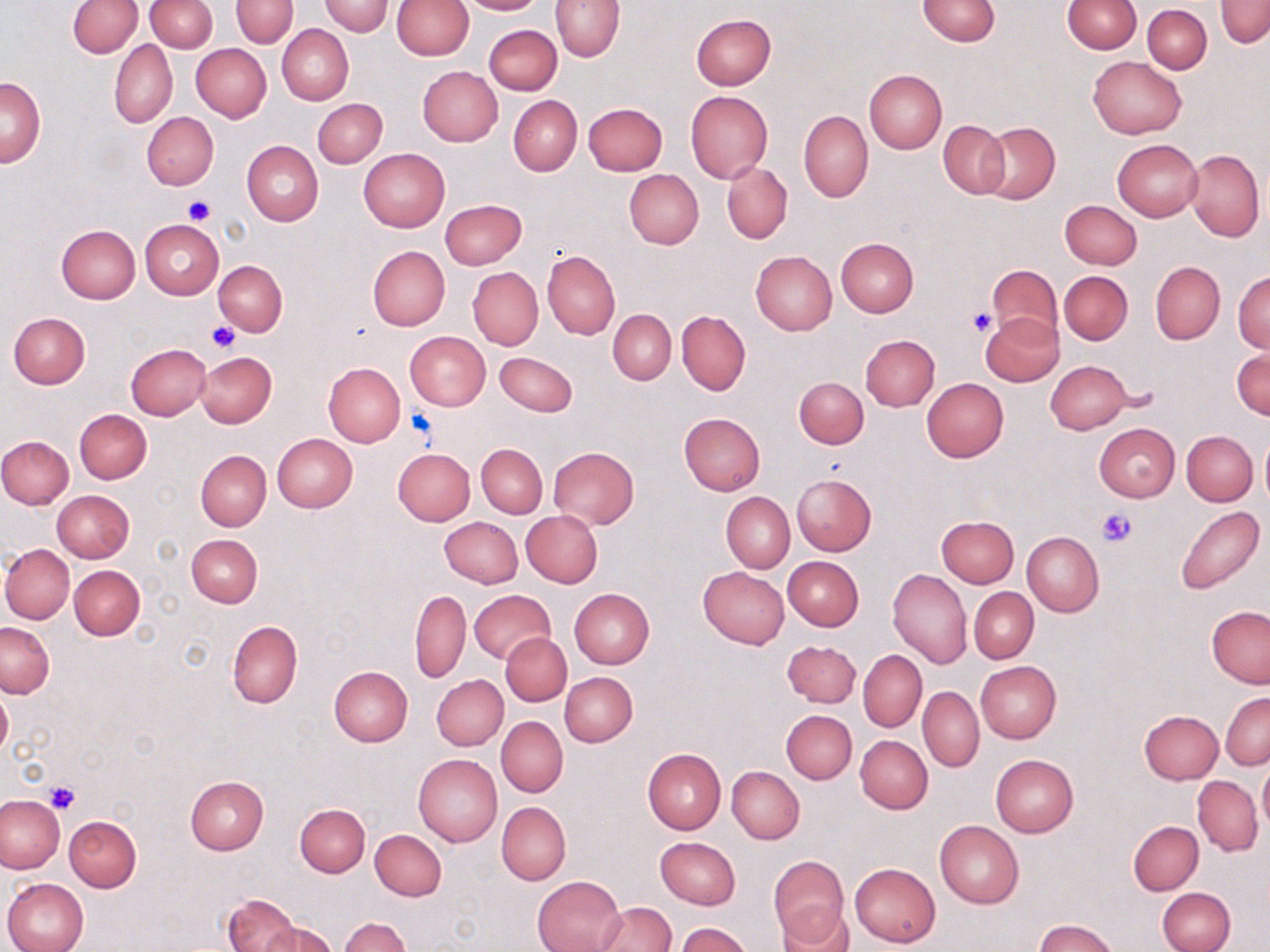

Approximate bounding boxes as named x1/y1/x2/y2 corners in pixels. Platelet locations: (x1=183, y1=197, x2=215, y2=224), (x1=968, y1=307, x2=997, y2=335), (x1=207, y1=321, x2=241, y2=352), (x1=406, y1=410, x2=435, y2=440), (x1=1097, y1=509, x2=1135, y2=548), (x1=42, y1=779, x2=82, y2=815). Uninfected red blood cell locations: (x1=145, y1=0, x2=217, y2=53), (x1=231, y1=0, x2=298, y2=48), (x1=460, y1=0, x2=542, y2=15), (x1=916, y1=0, x2=1000, y2=46), (x1=1062, y1=0, x2=1141, y2=53), (x1=1216, y1=0, x2=1270, y2=48), (x1=68, y1=1, x2=143, y2=58), (x1=319, y1=1, x2=392, y2=36), (x1=390, y1=1, x2=473, y2=59), (x1=551, y1=1, x2=624, y2=61), (x1=1142, y1=4, x2=1211, y2=73), (x1=691, y1=14, x2=775, y2=90), (x1=276, y1=24, x2=353, y2=105), (x1=484, y1=24, x2=562, y2=94), (x1=110, y1=40, x2=178, y2=127), (x1=191, y1=43, x2=271, y2=122), (x1=1088, y1=56, x2=1187, y2=139), (x1=417, y1=66, x2=503, y2=146), (x1=864, y1=69, x2=947, y2=153), (x1=1, y1=77, x2=45, y2=167), (x1=685, y1=90, x2=773, y2=184), (x1=508, y1=95, x2=581, y2=175), (x1=313, y1=98, x2=388, y2=168), (x1=583, y1=103, x2=668, y2=176), (x1=798, y1=110, x2=873, y2=202), (x1=141, y1=112, x2=219, y2=190), (x1=938, y1=120, x2=1010, y2=197), (x1=976, y1=122, x2=1060, y2=205), (x1=1112, y1=139, x2=1203, y2=222), (x1=241, y1=141, x2=323, y2=226), (x1=1184, y1=147, x2=1264, y2=242), (x1=358, y1=148, x2=449, y2=232), (x1=722, y1=162, x2=792, y2=244), (x1=624, y1=169, x2=702, y2=249), (x1=440, y1=199, x2=526, y2=269), (x1=449, y1=199, x2=529, y2=346), (x1=1060, y1=200, x2=1141, y2=269), (x1=140, y1=219, x2=223, y2=299), (x1=56, y1=224, x2=140, y2=303), (x1=835, y1=237, x2=918, y2=317), (x1=368, y1=247, x2=450, y2=329), (x1=542, y1=250, x2=620, y2=339), (x1=750, y1=250, x2=838, y2=335), (x1=214, y1=261, x2=286, y2=334), (x1=1149, y1=261, x2=1225, y2=346), (x1=987, y1=263, x2=1064, y2=343), (x1=468, y1=267, x2=543, y2=351), (x1=1234, y1=270, x2=1270, y2=353), (x1=1059, y1=271, x2=1132, y2=344), (x1=608, y1=309, x2=676, y2=384), (x1=676, y1=310, x2=750, y2=395), (x1=8, y1=311, x2=91, y2=388), (x1=980, y1=313, x2=1063, y2=386), (x1=404, y1=331, x2=490, y2=411), (x1=861, y1=335, x2=939, y2=410), (x1=125, y1=344, x2=211, y2=419), (x1=1232, y1=349, x2=1270, y2=420), (x1=194, y1=352, x2=276, y2=429), (x1=495, y1=352, x2=577, y2=417), (x1=1045, y1=360, x2=1133, y2=434), (x1=323, y1=363, x2=405, y2=446), (x1=794, y1=376, x2=868, y2=448), (x1=922, y1=377, x2=1008, y2=462), (x1=75, y1=409, x2=152, y2=483), (x1=678, y1=412, x2=765, y2=496), (x1=1094, y1=424, x2=1180, y2=502), (x1=1181, y1=430, x2=1257, y2=505), (x1=272, y1=433, x2=357, y2=512), (x1=1258, y1=433, x2=1270, y2=509), (x1=0, y1=435, x2=74, y2=508), (x1=477, y1=443, x2=548, y2=518), (x1=548, y1=447, x2=639, y2=529), (x1=392, y1=448, x2=474, y2=525), (x1=195, y1=450, x2=271, y2=531), (x1=792, y1=473, x2=877, y2=555), (x1=53, y1=491, x2=133, y2=562), (x1=721, y1=493, x2=794, y2=571), (x1=1173, y1=505, x2=1263, y2=595), (x1=521, y1=511, x2=603, y2=587), (x1=936, y1=515, x2=1019, y2=586), (x1=440, y1=516, x2=523, y2=588), (x1=1022, y1=532, x2=1104, y2=616), (x1=187, y1=533, x2=262, y2=607), (x1=1, y1=544, x2=74, y2=623), (x1=783, y1=556, x2=864, y2=631), (x1=69, y1=565, x2=144, y2=640), (x1=698, y1=566, x2=789, y2=649), (x1=887, y1=568, x2=971, y2=669), (x1=969, y1=587, x2=1038, y2=663), (x1=569, y1=588, x2=655, y2=669), (x1=410, y1=589, x2=471, y2=683), (x1=468, y1=589, x2=556, y2=664), (x1=1207, y1=605, x2=1270, y2=687), (x1=227, y1=621, x2=302, y2=708), (x1=0, y1=622, x2=54, y2=697), (x1=502, y1=633, x2=571, y2=706), (x1=784, y1=640, x2=861, y2=707), (x1=859, y1=650, x2=927, y2=731), (x1=976, y1=660, x2=1060, y2=744), (x1=328, y1=664, x2=413, y2=746), (x1=561, y1=672, x2=638, y2=746), (x1=432, y1=674, x2=508, y2=749), (x1=0, y1=687, x2=12, y2=758), (x1=919, y1=688, x2=984, y2=771), (x1=1220, y1=692, x2=1269, y2=770), (x1=782, y1=710, x2=857, y2=784), (x1=1138, y1=710, x2=1222, y2=785), (x1=497, y1=717, x2=567, y2=796), (x1=856, y1=735, x2=932, y2=813), (x1=643, y1=748, x2=726, y2=834), (x1=413, y1=754, x2=502, y2=847), (x1=990, y1=754, x2=1077, y2=838), (x1=1258, y1=759, x2=1270, y2=834), (x1=727, y1=766, x2=804, y2=843), (x1=1193, y1=775, x2=1263, y2=857), (x1=184, y1=776, x2=268, y2=854), (x1=0, y1=794, x2=67, y2=874), (x1=295, y1=802, x2=370, y2=877), (x1=497, y1=802, x2=570, y2=884), (x1=64, y1=815, x2=141, y2=891), (x1=934, y1=820, x2=1024, y2=907), (x1=1129, y1=821, x2=1203, y2=895), (x1=370, y1=829, x2=447, y2=901), (x1=655, y1=836, x2=741, y2=909), (x1=768, y1=856, x2=849, y2=946), (x1=850, y1=862, x2=940, y2=947), (x1=533, y1=875, x2=626, y2=952), (x1=2, y1=878, x2=88, y2=952), (x1=1158, y1=887, x2=1235, y2=952), (x1=223, y1=893, x2=300, y2=952), (x1=594, y1=901, x2=676, y2=951), (x1=776, y1=902, x2=856, y2=952), (x1=340, y1=917, x2=409, y2=951), (x1=1035, y1=919, x2=1117, y2=952), (x1=265, y1=921, x2=337, y2=952), (x1=677, y1=923, x2=752, y2=952). Slide-level diagnosis: no evidence of blood parasites. Thin blood smear. Single field of view. May-Grünwald-Giemsa-stained preparation. Captured at 1000x magnification. Light microscopy. Image is 1270×952 pixels.